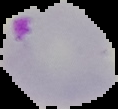

result: Plasmodium parasites identified
image_size: 118×109 pixels
image_type: cell region segmented out of the field of view; surrounding area masked to black
preparation: thin blood film